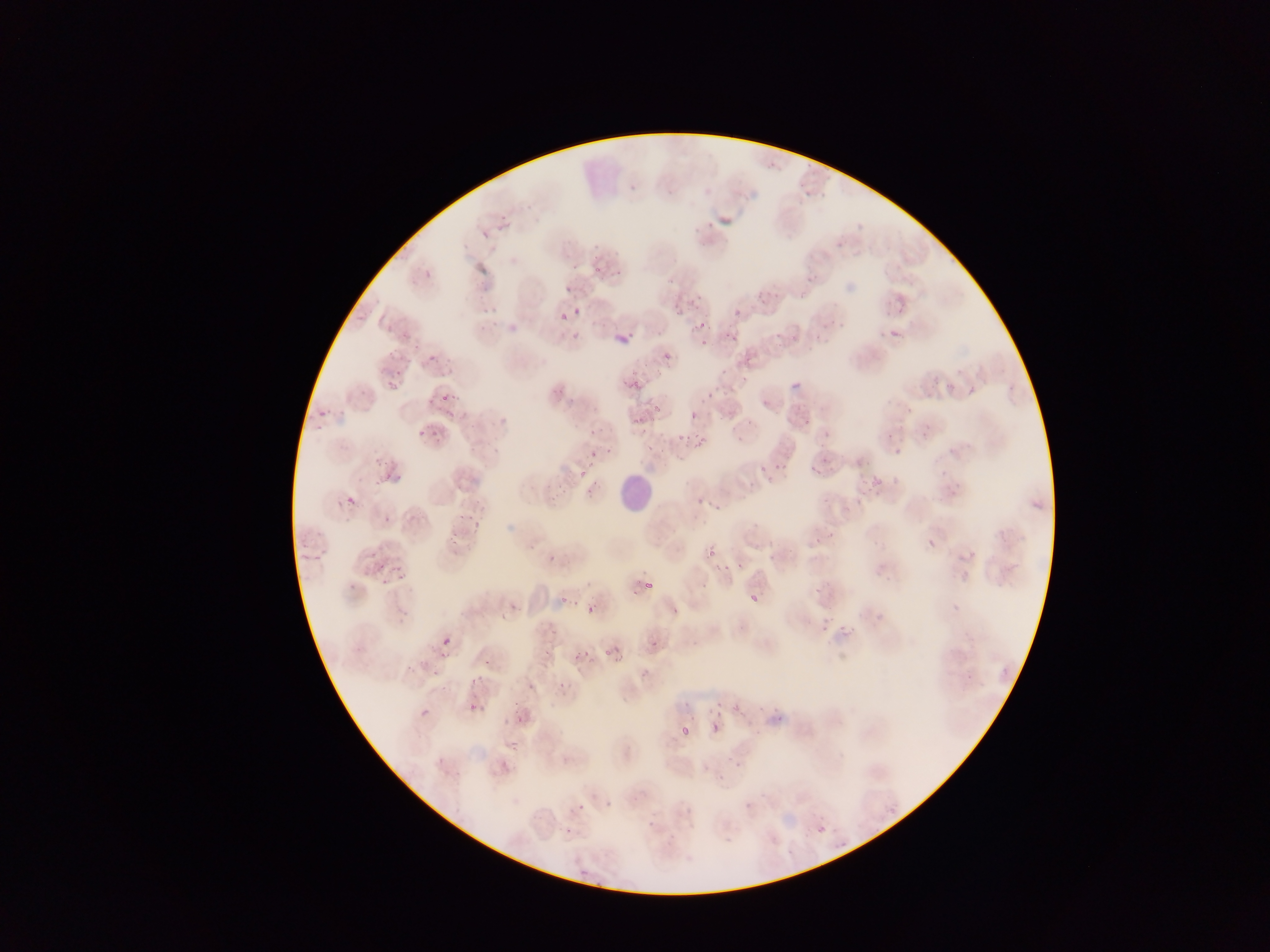
Approximate bounding boxes as [left, top, right, bottom] in pixels. Leukocyte locations: [615, 469, 657, 507]. Plasmodium parasite locations: [520, 207, 531, 216], [497, 212, 510, 223], [481, 228, 490, 241], [590, 250, 601, 260], [571, 260, 582, 272], [613, 268, 622, 277], [423, 269, 433, 283], [593, 269, 601, 275], [565, 285, 572, 293], [691, 302, 702, 313], [482, 306, 493, 315], [574, 306, 582, 317], [676, 307, 686, 315], [734, 307, 740, 316], [557, 314, 568, 325], [698, 321, 706, 330], [381, 322, 392, 333], [729, 330, 736, 341], [569, 331, 583, 342], [618, 333, 633, 345], [700, 339, 708, 346], [390, 346, 400, 360], [403, 352, 414, 366], [426, 354, 436, 364], [436, 364, 456, 384], [394, 369, 403, 382], [620, 378, 627, 387], [630, 378, 640, 387], [384, 379, 398, 387], [449, 393, 463, 401], [705, 393, 712, 401], [438, 396, 449, 407], [652, 402, 663, 412], [317, 409, 325, 417], [444, 411, 454, 421], [690, 412, 698, 420], [630, 417, 645, 428], [744, 420, 752, 427], [314, 426, 323, 435], [412, 429, 424, 439], [430, 429, 439, 439], [676, 433, 686, 442], [695, 435, 704, 448], [642, 442, 654, 453], [661, 443, 670, 457], [605, 445, 614, 453], [590, 447, 600, 457], [893, 448, 902, 457], [372, 456, 382, 465], [776, 460, 785, 471], [579, 462, 591, 478], [810, 465, 819, 475], [764, 468, 778, 486], [381, 471, 393, 479], [587, 473, 603, 494], [395, 474, 406, 487], [558, 486, 566, 493], [344, 495, 357, 506], [695, 497, 705, 511], [382, 514, 393, 527], [455, 514, 466, 525], [469, 521, 482, 533], [314, 528, 325, 540], [297, 539, 310, 550], [448, 539, 461, 551], [927, 539, 935, 549], [707, 546, 716, 556], [314, 553, 322, 565], [547, 553, 558, 565], [301, 554, 310, 563], [768, 554, 775, 562], [374, 561, 382, 571], [737, 562, 745, 571], [392, 564, 398, 573], [719, 565, 730, 573], [398, 576, 406, 586], [381, 577, 389, 587], [349, 580, 358, 591], [645, 581, 654, 590], [699, 585, 707, 593], [750, 594, 758, 602], [558, 595, 569, 609], [585, 605, 595, 614], [671, 606, 680, 615], [498, 611, 508, 619], [840, 624, 848, 632], [819, 626, 827, 634], [442, 636, 451, 646], [645, 636, 655, 649], [598, 646, 617, 656], [579, 648, 591, 660], [437, 654, 446, 662], [483, 660, 491, 669], [405, 666, 417, 676], [430, 668, 441, 677], [557, 680, 569, 691], [527, 681, 535, 690], [679, 698, 690, 707], [732, 701, 745, 715], [422, 703, 433, 717], [468, 703, 477, 712], [757, 703, 767, 709], [708, 705, 717, 713], [511, 709, 529, 724], [715, 713, 723, 717], [775, 715, 784, 723], [712, 722, 722, 732], [681, 727, 690, 737], [735, 762, 744, 773], [743, 801, 751, 809], [577, 804, 585, 813], [563, 827, 570, 835], [819, 827, 826, 835] | approximate [x, y] pixel centers of objects too small to bound: [668, 355], [594, 428], [358, 484], [377, 485], [454, 534], [375, 553], [720, 703], [777, 709]. One field of view. Mobile-phone photograph taken through the microscope. Collected in Ghana. Image is 1270×952 pixels. Thin blood smear.